Identify the blood parasite species.
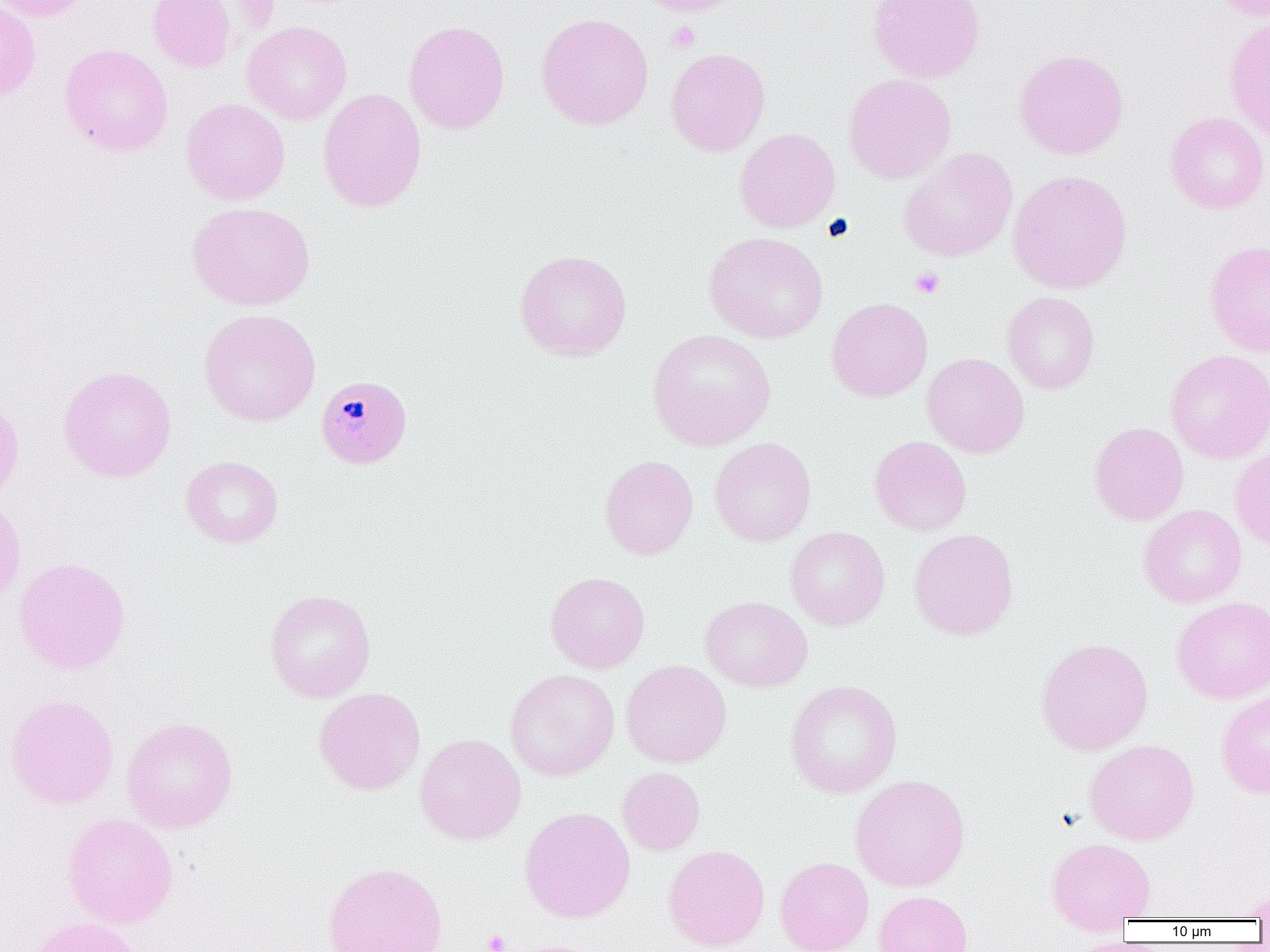
Plasmodium malariae.

field of view = single
platelet locations = approximate bounding boxes as named x1/y1/x2/y2 corners in pixels: (x1=667, y1=21, x2=700, y2=53), (x1=909, y1=266, x2=945, y2=299), (x1=482, y1=929, x2=510, y2=952)
magnification = 1000x
Plasmodium malariae-infected red blood cell locations = approximate bounding boxes as named x1/y1/x2/y2 corners in pixels: (x1=315, y1=374, x2=413, y2=470)
preparation = thin blood film
modality = optical microscopy
uninfected red blood cell locations = approximate bounding boxes as named x1/y1/x2/y2 corners in pixels: (x1=0, y1=0, x2=96, y2=22), (x1=148, y1=0, x2=237, y2=72), (x1=633, y1=0, x2=742, y2=16), (x1=867, y1=0, x2=986, y2=84), (x1=1211, y1=0, x2=1269, y2=22), (x1=0, y1=2, x2=41, y2=101), (x1=535, y1=13, x2=654, y2=130), (x1=1222, y1=18, x2=1270, y2=141), (x1=404, y1=20, x2=510, y2=135), (x1=242, y1=21, x2=352, y2=125), (x1=59, y1=44, x2=174, y2=157), (x1=666, y1=48, x2=770, y2=156), (x1=1013, y1=48, x2=1129, y2=159), (x1=843, y1=73, x2=956, y2=183), (x1=318, y1=88, x2=427, y2=213), (x1=181, y1=99, x2=290, y2=205), (x1=1165, y1=111, x2=1269, y2=214), (x1=735, y1=128, x2=840, y2=233), (x1=899, y1=148, x2=1018, y2=262), (x1=1008, y1=170, x2=1132, y2=294), (x1=187, y1=202, x2=315, y2=311), (x1=704, y1=232, x2=828, y2=343), (x1=1204, y1=240, x2=1270, y2=357), (x1=514, y1=250, x2=632, y2=361), (x1=1002, y1=292, x2=1099, y2=394), (x1=826, y1=297, x2=933, y2=402), (x1=198, y1=309, x2=321, y2=427), (x1=647, y1=329, x2=776, y2=451), (x1=1165, y1=349, x2=1270, y2=464), (x1=922, y1=353, x2=1029, y2=457), (x1=57, y1=365, x2=177, y2=482), (x1=0, y1=397, x2=24, y2=505), (x1=1090, y1=422, x2=1189, y2=525), (x1=869, y1=436, x2=971, y2=536), (x1=709, y1=437, x2=816, y2=547), (x1=1230, y1=448, x2=1270, y2=550), (x1=599, y1=455, x2=698, y2=559), (x1=181, y1=456, x2=283, y2=548), (x1=0, y1=493, x2=27, y2=609), (x1=1138, y1=504, x2=1246, y2=608), (x1=786, y1=526, x2=890, y2=630), (x1=909, y1=528, x2=1018, y2=640), (x1=13, y1=557, x2=131, y2=675), (x1=545, y1=571, x2=650, y2=673), (x1=265, y1=589, x2=376, y2=702), (x1=700, y1=596, x2=813, y2=692), (x1=1171, y1=596, x2=1270, y2=703), (x1=1036, y1=638, x2=1153, y2=755), (x1=621, y1=659, x2=731, y2=768), (x1=505, y1=669, x2=619, y2=780), (x1=784, y1=679, x2=903, y2=798), (x1=314, y1=687, x2=425, y2=795), (x1=1216, y1=690, x2=1270, y2=799), (x1=4, y1=693, x2=119, y2=809), (x1=121, y1=717, x2=238, y2=834), (x1=415, y1=733, x2=526, y2=844), (x1=1084, y1=739, x2=1199, y2=845), (x1=617, y1=766, x2=705, y2=855), (x1=849, y1=774, x2=970, y2=892), (x1=519, y1=807, x2=636, y2=923), (x1=62, y1=813, x2=179, y2=928), (x1=1046, y1=837, x2=1156, y2=931), (x1=663, y1=844, x2=770, y2=951), (x1=775, y1=857, x2=873, y2=952), (x1=322, y1=861, x2=448, y2=952), (x1=1237, y1=887, x2=1270, y2=920), (x1=874, y1=890, x2=973, y2=952), (x1=26, y1=917, x2=146, y2=952), (x1=1062, y1=937, x2=1148, y2=952), (x1=498, y1=939, x2=612, y2=952)
image size = 1270×952 pixels